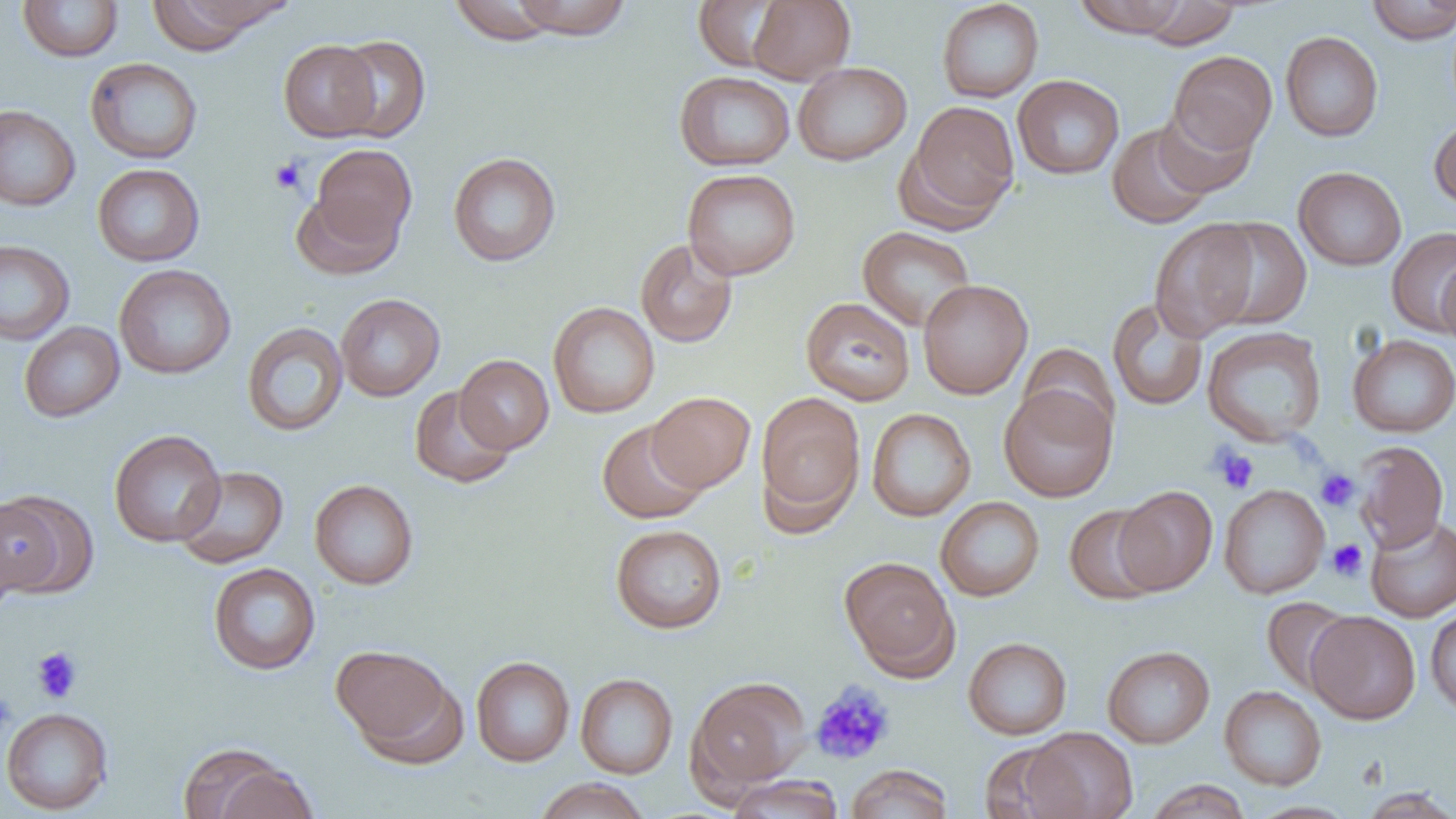

slide-level diagnosis = no evidence of blood parasites
image size = 1456×819 pixels
field of view = one of a larger specimen
uninfected red blood cell locations = approximate bounding boxes as named x1/y1/x2/y2 corners in pixels: (x1=17, y1=0, x2=124, y2=62), (x1=147, y1=0, x2=292, y2=50), (x1=509, y1=0, x2=632, y2=40), (x1=748, y1=0, x2=855, y2=84), (x1=937, y1=0, x2=1044, y2=103), (x1=1074, y1=0, x2=1191, y2=37), (x1=1366, y1=0, x2=1456, y2=44), (x1=448, y1=1, x2=561, y2=45), (x1=693, y1=1, x2=790, y2=72), (x1=1136, y1=1, x2=1241, y2=49), (x1=1280, y1=31, x2=1383, y2=142), (x1=331, y1=35, x2=431, y2=144), (x1=278, y1=39, x2=381, y2=141), (x1=1168, y1=50, x2=1277, y2=155), (x1=85, y1=58, x2=203, y2=164), (x1=792, y1=61, x2=911, y2=166), (x1=674, y1=71, x2=795, y2=171), (x1=1012, y1=75, x2=1125, y2=179), (x1=903, y1=101, x2=1020, y2=228), (x1=0, y1=105, x2=81, y2=212), (x1=1155, y1=106, x2=1257, y2=198), (x1=1429, y1=115, x2=1456, y2=211), (x1=1108, y1=122, x2=1214, y2=229), (x1=309, y1=144, x2=417, y2=252), (x1=448, y1=152, x2=561, y2=266), (x1=92, y1=163, x2=205, y2=267), (x1=1293, y1=166, x2=1407, y2=271), (x1=682, y1=168, x2=801, y2=280), (x1=291, y1=188, x2=404, y2=280), (x1=1204, y1=217, x2=1312, y2=331), (x1=1149, y1=218, x2=1261, y2=341), (x1=858, y1=226, x2=976, y2=331), (x1=1386, y1=227, x2=1456, y2=336), (x1=635, y1=239, x2=737, y2=348), (x1=0, y1=240, x2=75, y2=346), (x1=1436, y1=259, x2=1456, y2=348), (x1=114, y1=264, x2=236, y2=379), (x1=918, y1=279, x2=1033, y2=399), (x1=335, y1=293, x2=445, y2=401), (x1=800, y1=297, x2=915, y2=406), (x1=1108, y1=298, x2=1209, y2=411), (x1=548, y1=301, x2=660, y2=418), (x1=19, y1=321, x2=124, y2=422), (x1=241, y1=321, x2=348, y2=437), (x1=1202, y1=326, x2=1327, y2=446), (x1=1348, y1=334, x2=1456, y2=437), (x1=1018, y1=342, x2=1120, y2=440), (x1=455, y1=354, x2=555, y2=454), (x1=999, y1=383, x2=1117, y2=502), (x1=409, y1=385, x2=517, y2=488), (x1=646, y1=391, x2=756, y2=492), (x1=755, y1=392, x2=866, y2=527), (x1=866, y1=407, x2=976, y2=521), (x1=597, y1=419, x2=709, y2=524), (x1=108, y1=429, x2=225, y2=547), (x1=1353, y1=440, x2=1449, y2=552), (x1=173, y1=466, x2=289, y2=568), (x1=309, y1=479, x2=419, y2=590), (x1=1219, y1=484, x2=1329, y2=599), (x1=1114, y1=486, x2=1218, y2=595), (x1=0, y1=492, x2=84, y2=599), (x1=935, y1=496, x2=1045, y2=601), (x1=1063, y1=504, x2=1166, y2=605), (x1=1365, y1=515, x2=1456, y2=622), (x1=610, y1=524, x2=727, y2=634), (x1=840, y1=557, x2=958, y2=677), (x1=208, y1=563, x2=321, y2=674), (x1=1261, y1=598, x2=1357, y2=697), (x1=1425, y1=604, x2=1456, y2=717), (x1=1305, y1=610, x2=1421, y2=724), (x1=963, y1=637, x2=1072, y2=739), (x1=331, y1=643, x2=460, y2=758), (x1=1102, y1=645, x2=1215, y2=748), (x1=471, y1=656, x2=574, y2=766), (x1=575, y1=673, x2=678, y2=779), (x1=687, y1=676, x2=812, y2=792), (x1=1220, y1=685, x2=1326, y2=790), (x1=1, y1=707, x2=114, y2=815), (x1=1022, y1=727, x2=1138, y2=818), (x1=978, y1=741, x2=1077, y2=818), (x1=180, y1=744, x2=313, y2=819), (x1=845, y1=763, x2=954, y2=819), (x1=726, y1=775, x2=844, y2=819), (x1=533, y1=777, x2=651, y2=819), (x1=1146, y1=779, x2=1251, y2=819), (x1=1357, y1=788, x2=1456, y2=818)
modality = optical microscopy
preparation = thin blood film
magnification = 1000x
platelet locations = approximate bounding boxes as named x1/y1/x2/y2 corners in pixels: (x1=269, y1=157, x2=306, y2=194), (x1=1211, y1=445, x2=1260, y2=494), (x1=1315, y1=468, x2=1360, y2=512), (x1=1327, y1=539, x2=1368, y2=581), (x1=31, y1=647, x2=82, y2=703), (x1=809, y1=681, x2=896, y2=765), (x1=0, y1=691, x2=16, y2=739)